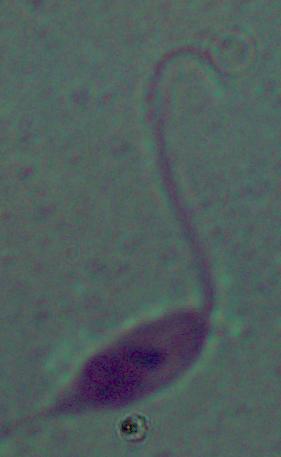

magnification = 1000x
identification = Leishmania
modality = micrograph